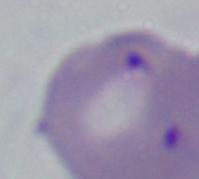 A Babesia parasite is seen. Captured at 1000x magnification. Photomicrograph.